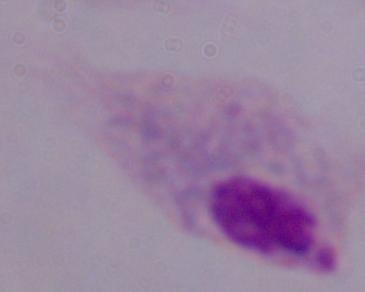

1000x magnification. Photomicrograph. A trichomonad is shown.